Assess the morphology of the erythrocytes.
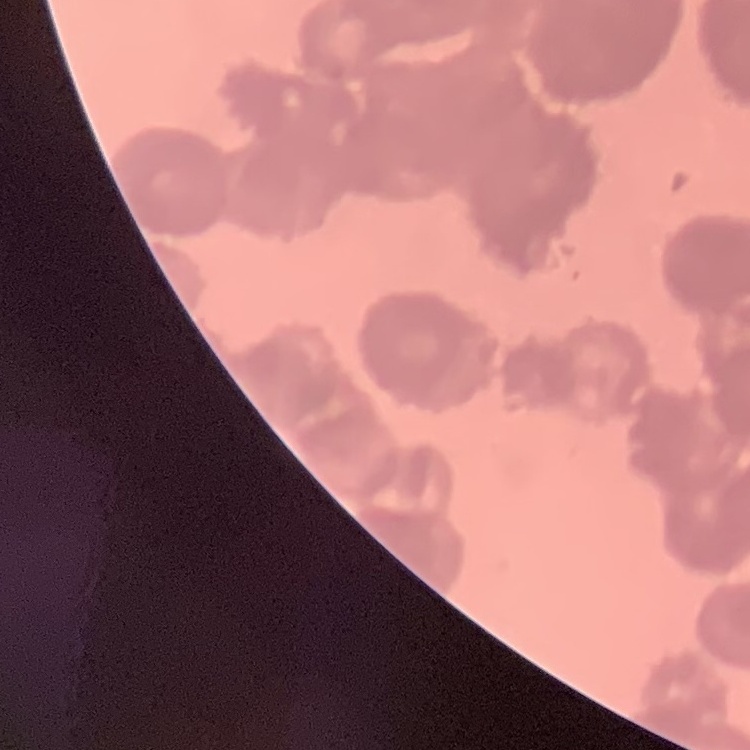
Rouleaux formation.

Thin blood smear. Square crop of a larger photomicrograph. Stained with either Field's or Giemsa.